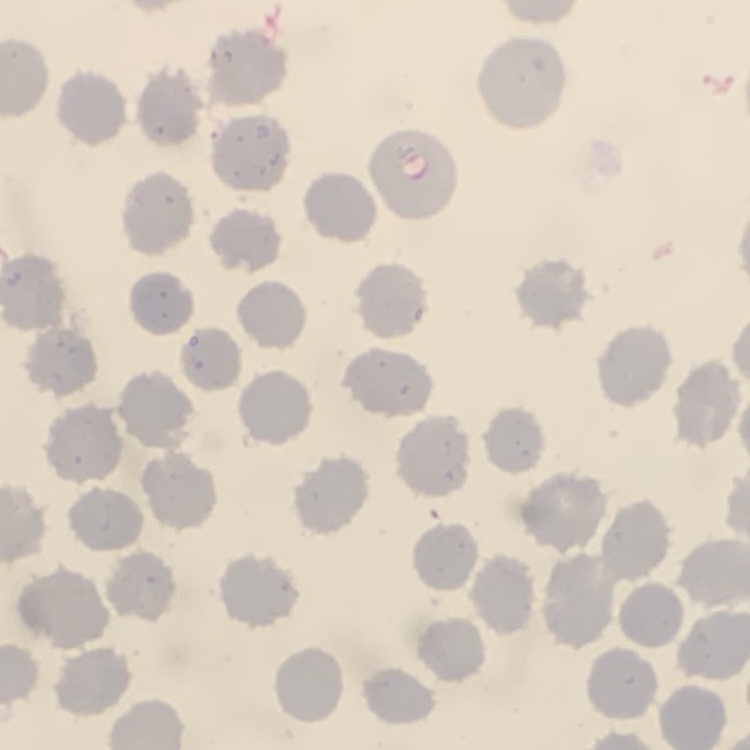 The red blood cells show no rouleaux formation. Field's or Giemsa stain. Square crop of a larger photomicrograph. Thin blood smear.